Locate and identify every blood parasite.
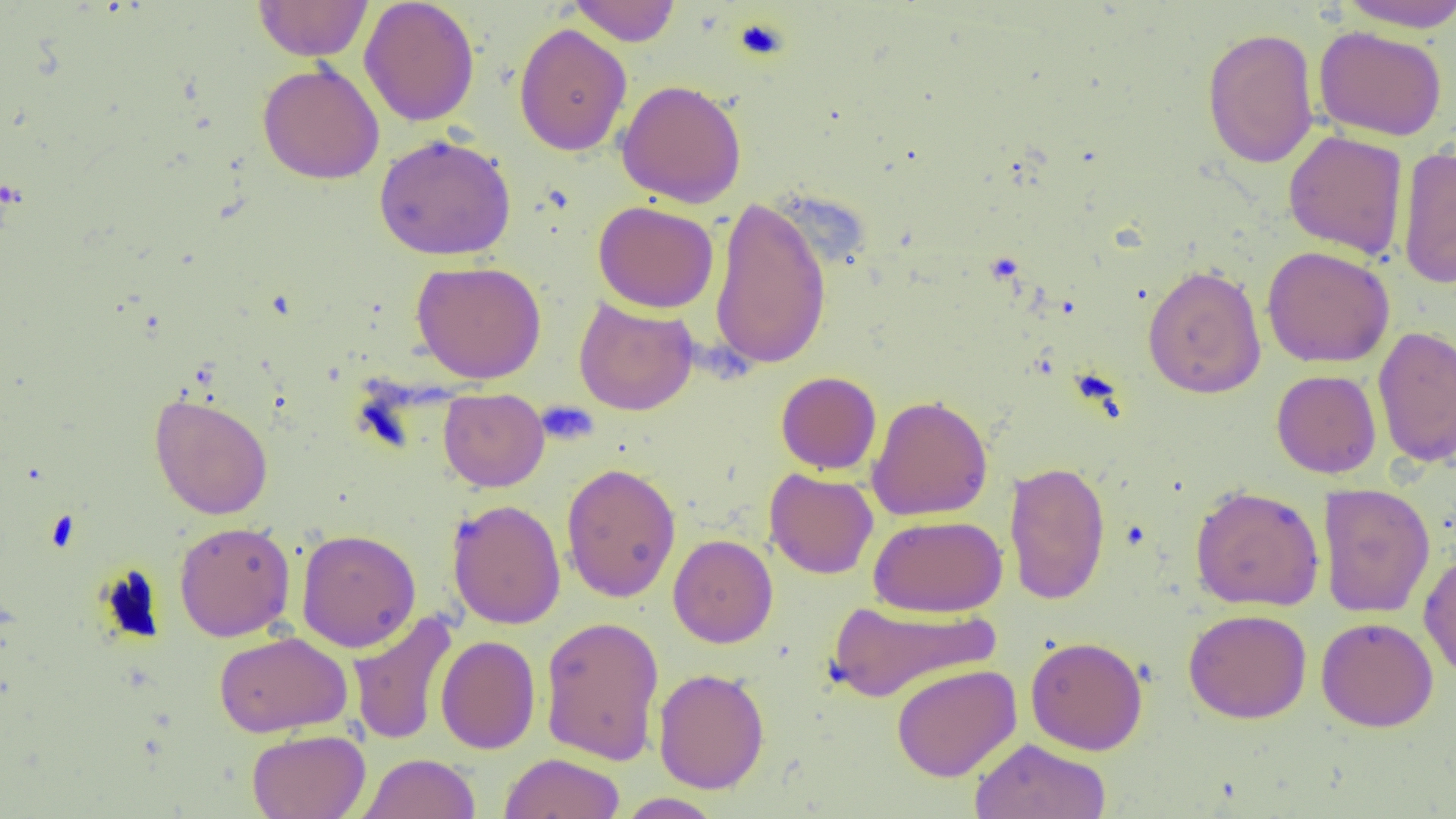
No blood parasites seen.

Summary:
  - Coordinate format: approximate bounding boxes as named x1/y1/x2/y2 corners in pixels
  - Uninfected red blood cell locations: (x1=359, y1=0, x2=480, y2=127), (x1=568, y1=0, x2=682, y2=46), (x1=254, y1=1, x2=373, y2=61), (x1=1335, y1=1, x2=1456, y2=32), (x1=514, y1=23, x2=632, y2=156), (x1=1314, y1=26, x2=1448, y2=141), (x1=1201, y1=27, x2=1319, y2=169), (x1=257, y1=62, x2=385, y2=185), (x1=617, y1=79, x2=747, y2=207), (x1=1283, y1=130, x2=1408, y2=260), (x1=374, y1=132, x2=517, y2=261), (x1=1396, y1=144, x2=1456, y2=289), (x1=709, y1=194, x2=832, y2=371), (x1=593, y1=201, x2=719, y2=313), (x1=1261, y1=246, x2=1395, y2=368), (x1=1139, y1=258, x2=1394, y2=380), (x1=411, y1=260, x2=547, y2=383), (x1=1142, y1=264, x2=1267, y2=399), (x1=574, y1=298, x2=698, y2=415), (x1=1372, y1=325, x2=1456, y2=467), (x1=1271, y1=369, x2=1381, y2=478), (x1=776, y1=371, x2=881, y2=474), (x1=438, y1=388, x2=549, y2=492), (x1=149, y1=393, x2=273, y2=520), (x1=867, y1=394, x2=993, y2=522), (x1=1004, y1=460, x2=1111, y2=605), (x1=560, y1=462, x2=682, y2=603), (x1=764, y1=468, x2=879, y2=579), (x1=1318, y1=482, x2=1435, y2=618), (x1=1190, y1=484, x2=1325, y2=612), (x1=447, y1=498, x2=566, y2=630), (x1=869, y1=514, x2=1007, y2=617), (x1=174, y1=521, x2=295, y2=641), (x1=296, y1=528, x2=421, y2=652), (x1=668, y1=534, x2=778, y2=648), (x1=1418, y1=549, x2=1456, y2=682), (x1=826, y1=599, x2=999, y2=703), (x1=1183, y1=608, x2=1312, y2=723), (x1=348, y1=611, x2=458, y2=746), (x1=539, y1=615, x2=665, y2=765), (x1=1316, y1=616, x2=1439, y2=732), (x1=214, y1=630, x2=353, y2=737), (x1=436, y1=634, x2=540, y2=754), (x1=1025, y1=636, x2=1148, y2=755), (x1=891, y1=664, x2=1022, y2=782), (x1=653, y1=667, x2=770, y2=794), (x1=247, y1=728, x2=371, y2=818), (x1=969, y1=737, x2=1111, y2=818), (x1=500, y1=752, x2=625, y2=819), (x1=358, y1=753, x2=481, y2=819), (x1=616, y1=793, x2=725, y2=818)
  - Platelet locations: (x1=732, y1=16, x2=792, y2=63), (x1=537, y1=401, x2=599, y2=444)
  - Slide-level diagnosis: no evidence of blood parasites
  - Magnification: 1000x
  - Image size: 1456×819 pixels
  - Preparation: thin blood smear
  - Modality: light microscopy
  - Field of view: one of a larger specimen